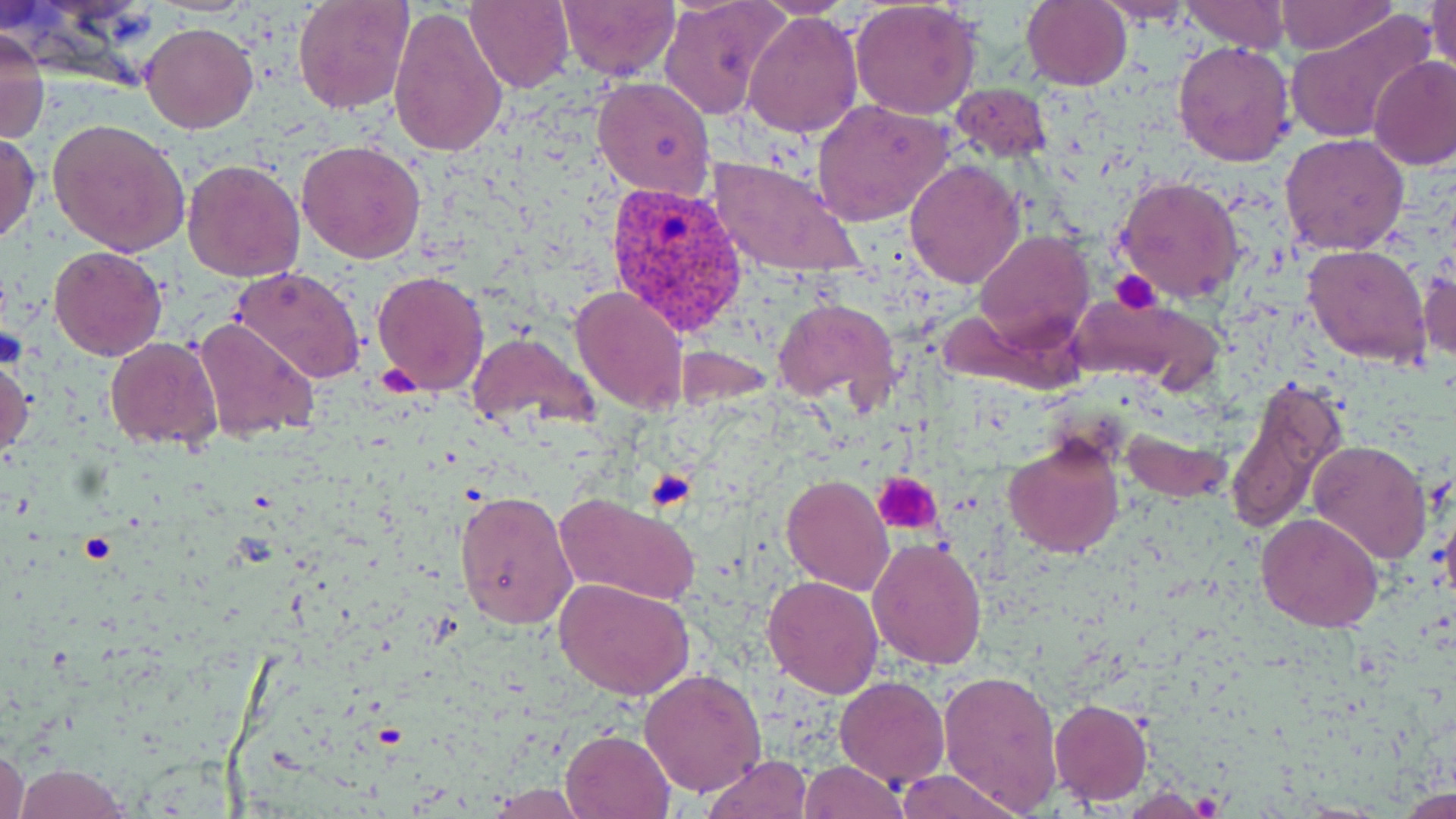

Summary:
  - Coordinate format: approximate bounding boxes as named x1/y1/x2/y2 corners in pixels
  - Uninfected red blood cell locations: (x1=292, y1=0, x2=414, y2=115), (x1=465, y1=0, x2=576, y2=94), (x1=557, y1=0, x2=678, y2=80), (x1=658, y1=0, x2=789, y2=121), (x1=753, y1=0, x2=860, y2=18), (x1=1182, y1=0, x2=1288, y2=52), (x1=1274, y1=0, x2=1398, y2=55), (x1=1427, y1=0, x2=1455, y2=80), (x1=849, y1=1, x2=981, y2=118), (x1=1021, y1=1, x2=1131, y2=90), (x1=1097, y1=1, x2=1195, y2=28), (x1=388, y1=7, x2=509, y2=160), (x1=743, y1=9, x2=863, y2=139), (x1=1283, y1=11, x2=1434, y2=145), (x1=139, y1=22, x2=258, y2=134), (x1=0, y1=25, x2=50, y2=147), (x1=1172, y1=42, x2=1296, y2=167), (x1=1367, y1=57, x2=1456, y2=171), (x1=593, y1=76, x2=716, y2=199), (x1=953, y1=83, x2=1052, y2=164), (x1=812, y1=99, x2=954, y2=226), (x1=49, y1=116, x2=191, y2=256), (x1=0, y1=127, x2=41, y2=244), (x1=1279, y1=133, x2=1410, y2=256), (x1=296, y1=139, x2=426, y2=263), (x1=711, y1=156, x2=861, y2=280), (x1=183, y1=158, x2=304, y2=281), (x1=904, y1=158, x2=1026, y2=288), (x1=1114, y1=174, x2=1245, y2=304), (x1=974, y1=230, x2=1094, y2=352), (x1=1302, y1=243, x2=1433, y2=368), (x1=48, y1=245, x2=167, y2=362), (x1=1419, y1=259, x2=1456, y2=370), (x1=231, y1=267, x2=367, y2=385), (x1=371, y1=269, x2=489, y2=395), (x1=569, y1=285, x2=688, y2=414), (x1=1068, y1=296, x2=1214, y2=389), (x1=779, y1=297, x2=898, y2=407), (x1=192, y1=318, x2=320, y2=444), (x1=467, y1=332, x2=598, y2=435), (x1=104, y1=336, x2=225, y2=452), (x1=0, y1=350, x2=33, y2=465), (x1=1225, y1=374, x2=1346, y2=536), (x1=1117, y1=424, x2=1230, y2=505), (x1=1002, y1=436, x2=1126, y2=556), (x1=1308, y1=440, x2=1432, y2=565), (x1=781, y1=474, x2=894, y2=594), (x1=455, y1=491, x2=578, y2=628), (x1=553, y1=493, x2=701, y2=607), (x1=1256, y1=513, x2=1383, y2=631), (x1=867, y1=536, x2=989, y2=670), (x1=762, y1=574, x2=886, y2=697), (x1=554, y1=579, x2=697, y2=700), (x1=937, y1=668, x2=1064, y2=812), (x1=640, y1=669, x2=766, y2=796), (x1=834, y1=677, x2=950, y2=786), (x1=1049, y1=698, x2=1151, y2=803), (x1=558, y1=727, x2=675, y2=819), (x1=0, y1=742, x2=28, y2=819), (x1=703, y1=754, x2=814, y2=818), (x1=799, y1=759, x2=907, y2=819), (x1=12, y1=763, x2=135, y2=818), (x1=897, y1=769, x2=1024, y2=819), (x1=482, y1=785, x2=593, y2=818), (x1=1399, y1=786, x2=1453, y2=817)
  - Platelet locations: (x1=1112, y1=269, x2=1163, y2=314), (x1=380, y1=365, x2=422, y2=400), (x1=643, y1=469, x2=694, y2=512), (x1=874, y1=472, x2=943, y2=535)
  - Plasmodium vivax-infected red blood cell locations: (x1=606, y1=182, x2=752, y2=342)
  - Slide-level diagnosis: Plasmodium vivax
  - Magnification: 1000x
  - Preparation: thin blood film
  - Stain: May-Grünwald-Giemsa
  - Field of view: single
  - Modality: light microscopy
  - Image size: 1456×819 pixels